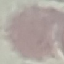

{
  "malaria_status": "uninfected",
  "preparation": "thin blood smear",
  "image_type": "automatically extracted cell patch, resized to 64 × 64 pixels",
  "capture": "smartphone through the microscope eyepiece",
  "stain": "Giemsa"
}